Find each cell and give its type.
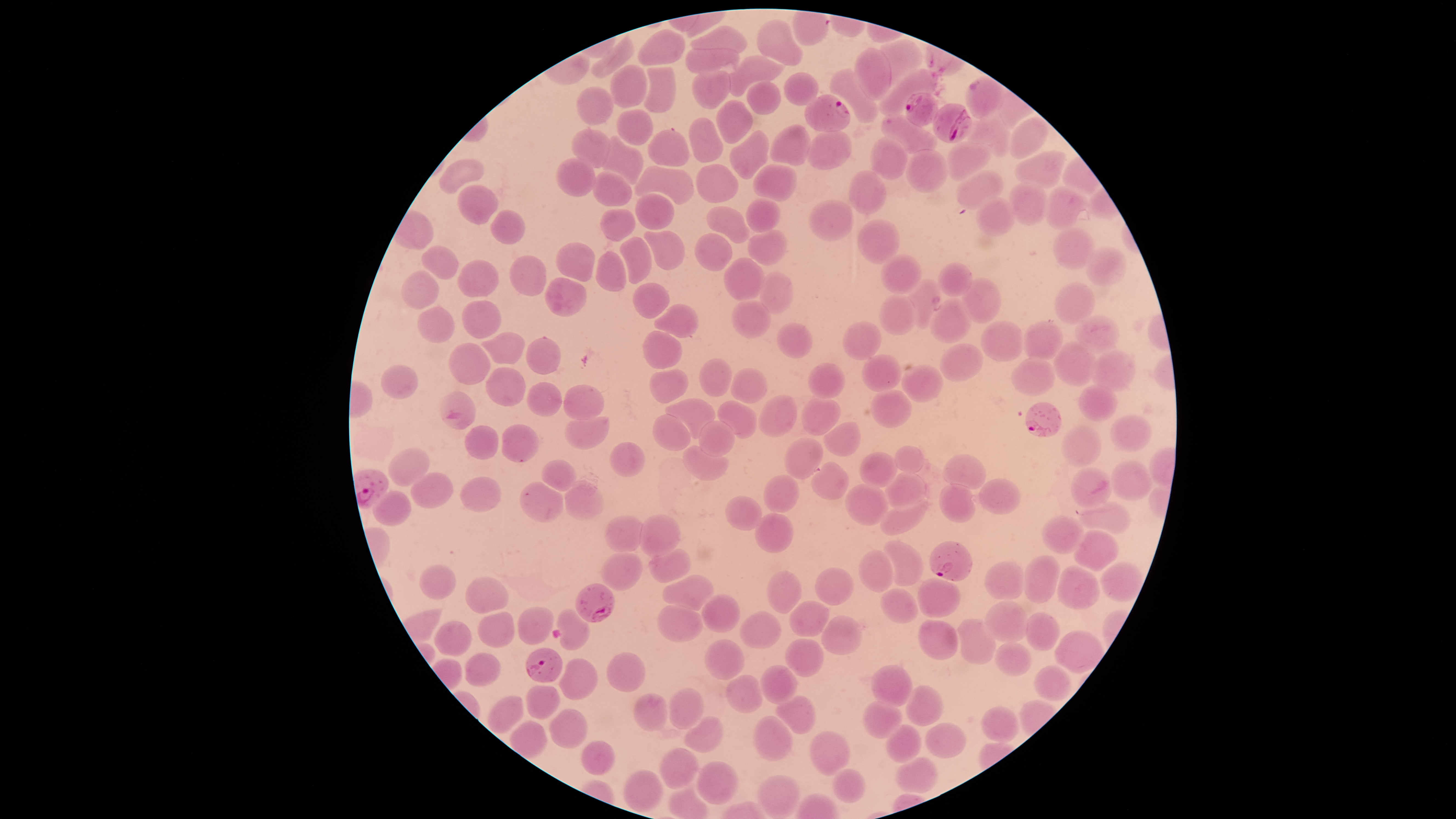
Approximate bounding boxes as [left, top, right, bottom] in pixels.
Parasitized red blood cells: [965, 76, 1001, 116], [905, 92, 937, 126], [804, 94, 851, 132], [933, 103, 972, 144], [1026, 402, 1061, 438], [930, 541, 971, 581], [575, 583, 614, 622], [526, 648, 562, 682].
Uninfected red blood cells: [755, 20, 802, 65], [690, 26, 746, 52], [637, 30, 685, 67], [590, 35, 633, 77], [877, 39, 922, 85], [686, 48, 739, 73], [854, 48, 890, 100], [721, 57, 784, 96], [610, 64, 649, 108], [643, 66, 677, 113], [830, 69, 878, 124], [691, 70, 731, 110], [877, 70, 939, 117], [784, 73, 818, 105], [747, 81, 781, 115], [576, 86, 613, 125], [717, 100, 753, 143], [617, 110, 653, 145], [881, 115, 935, 155], [688, 118, 724, 163], [1008, 118, 1051, 160], [964, 120, 1015, 158], [770, 125, 810, 165], [805, 128, 852, 170], [571, 129, 611, 167], [647, 129, 689, 167], [729, 130, 770, 179], [600, 134, 644, 185], [870, 136, 909, 178], [946, 141, 991, 182], [906, 149, 948, 193], [1016, 150, 1063, 188], [440, 157, 484, 194], [556, 158, 595, 197], [752, 164, 797, 202], [634, 165, 693, 204], [696, 165, 739, 203], [849, 169, 886, 214], [956, 170, 1002, 210], [592, 172, 632, 207], [1007, 182, 1049, 226], [457, 185, 498, 224], [1046, 187, 1090, 231], [635, 193, 675, 228], [977, 197, 1015, 235], [746, 198, 780, 233], [808, 200, 853, 242], [706, 206, 749, 244], [491, 209, 524, 244], [600, 209, 635, 241], [857, 219, 901, 264], [1053, 227, 1095, 271], [644, 229, 684, 271], [746, 229, 787, 266], [694, 233, 734, 272], [620, 237, 653, 283], [557, 242, 594, 282], [422, 245, 457, 279], [1086, 246, 1126, 287], [594, 252, 626, 292], [509, 254, 548, 297], [881, 255, 920, 294], [724, 257, 766, 301], [457, 261, 501, 297], [938, 263, 973, 298], [400, 271, 439, 309], [759, 272, 793, 314], [961, 276, 1000, 323], [544, 277, 587, 317], [908, 277, 942, 329], [631, 282, 670, 318], [1054, 282, 1098, 325], [879, 293, 919, 335], [928, 297, 972, 345], [731, 299, 771, 338], [462, 301, 502, 338], [655, 304, 699, 338], [417, 306, 455, 343], [1073, 315, 1121, 351], [980, 320, 1024, 362], [843, 321, 881, 360], [1024, 321, 1064, 363], [777, 323, 813, 357], [643, 329, 681, 369], [481, 331, 524, 366], [525, 338, 561, 375], [1053, 340, 1096, 386], [447, 343, 490, 385], [941, 343, 983, 385], [1091, 351, 1135, 387], [858, 353, 901, 392], [698, 358, 732, 397], [1012, 359, 1056, 394], [808, 362, 845, 400], [381, 364, 418, 399], [902, 365, 945, 404], [486, 367, 526, 407], [731, 368, 767, 404], [648, 370, 688, 404], [527, 381, 562, 417], [1078, 384, 1119, 421], [561, 386, 605, 419], [869, 389, 912, 429], [439, 390, 475, 430], [758, 393, 797, 439], [800, 395, 840, 436], [664, 399, 716, 438], [717, 400, 758, 439], [652, 414, 692, 451], [1110, 414, 1152, 453], [563, 417, 611, 449], [698, 421, 735, 457], [824, 421, 863, 456], [464, 425, 498, 460], [500, 425, 537, 461], [1061, 427, 1101, 467], [784, 438, 822, 479], [610, 441, 645, 478], [682, 444, 728, 481], [894, 445, 923, 473], [388, 448, 430, 486], [860, 452, 897, 489], [942, 454, 986, 488], [540, 459, 575, 491], [1112, 460, 1153, 499], [810, 463, 848, 499], [1071, 466, 1112, 507], [410, 471, 455, 508], [885, 472, 928, 508], [763, 474, 799, 513], [460, 476, 500, 512], [979, 478, 1021, 514], [520, 481, 563, 523], [565, 481, 603, 522], [940, 483, 975, 524], [844, 484, 888, 525], [374, 492, 411, 527], [880, 494, 928, 535], [725, 495, 762, 532], [1079, 500, 1135, 534], [638, 513, 680, 557], [754, 513, 794, 554], [605, 516, 645, 552], [1042, 516, 1084, 554], [1072, 531, 1119, 570], [884, 540, 923, 587], [649, 550, 690, 583], [857, 550, 895, 593], [600, 554, 641, 591], [1021, 556, 1059, 603], [1100, 561, 1145, 601], [983, 562, 1024, 599], [420, 564, 456, 600], [1057, 565, 1099, 610], [815, 568, 854, 606], [767, 571, 801, 614], [661, 574, 713, 608], [465, 577, 508, 614], [917, 579, 961, 617], [881, 588, 919, 624], [701, 595, 741, 632], [983, 600, 1028, 642], [790, 601, 829, 636], [657, 605, 704, 643], [518, 607, 554, 646], [557, 609, 590, 650], [740, 611, 782, 648], [1024, 612, 1059, 651], [478, 613, 516, 647], [821, 615, 863, 655], [955, 618, 998, 664], [917, 620, 958, 660], [433, 621, 471, 657], [1054, 630, 1104, 674], [784, 638, 824, 677], [704, 639, 745, 680], [993, 642, 1030, 677], [465, 652, 501, 685], [606, 652, 647, 693], [560, 658, 600, 701], [1035, 664, 1071, 700], [759, 665, 798, 704], [870, 665, 912, 706], [726, 675, 763, 712], [907, 685, 943, 726], [527, 686, 559, 718], [669, 688, 704, 727], [632, 693, 667, 731], [487, 695, 523, 733], [777, 696, 816, 733], [862, 700, 901, 739], [980, 706, 1018, 742], [549, 709, 586, 749], [753, 716, 792, 762], [684, 717, 724, 753], [510, 721, 547, 757], [924, 722, 967, 758], [884, 725, 922, 764], [810, 732, 850, 776], [581, 740, 615, 776], [658, 748, 700, 789], [894, 756, 939, 793], [697, 761, 737, 804], [622, 768, 666, 812], [831, 768, 866, 803], [756, 775, 800, 819].
No white blood cells identified.

Summary:
  - Image size: 1456×819 pixels
  - Species: Plasmodium falciparum
  - Capture: smartphone photograph through the microscope eyepiece
  - Preparation: thin blood film
  - Visible region: circular
  - Stain: Giemsa
  - Field of view: single